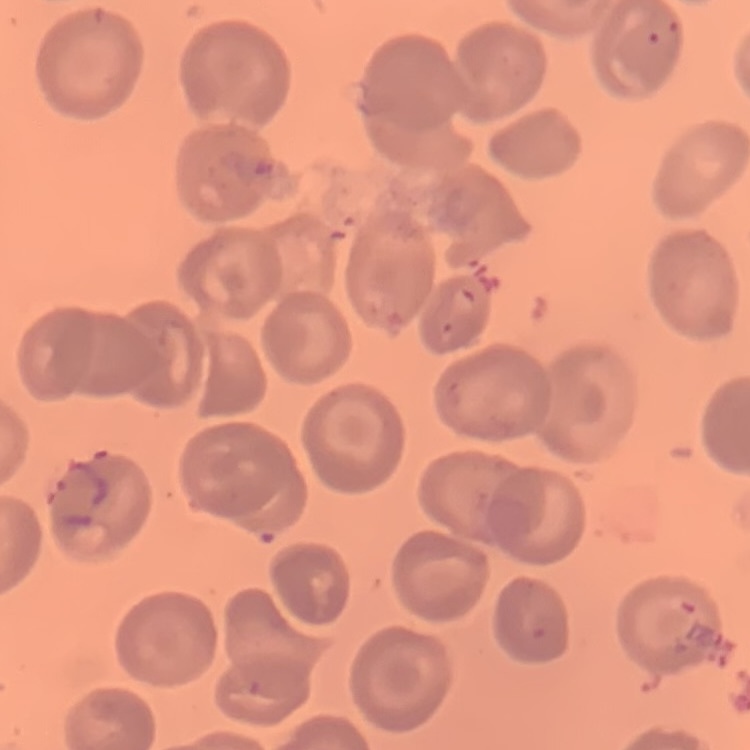

red blood cell morphology = no rouleaux formation
stain = Field's or Giemsa
image type = square crop of a larger photomicrograph
preparation = thin blood smear